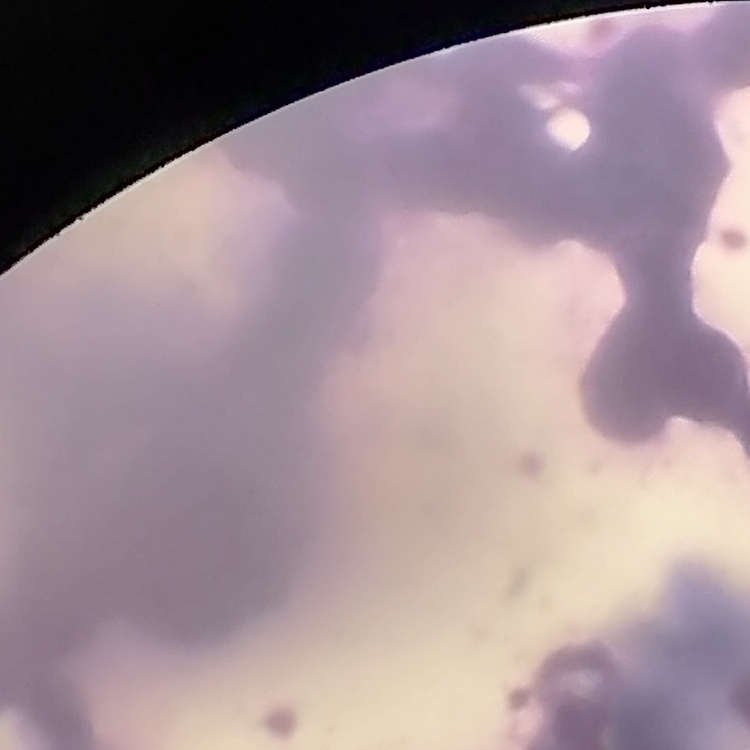
The erythrocytes show rouleaux formation. Field's or Giemsa stain. Thin blood film. One tile cut from a larger photomicrograph.